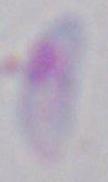

modality: micrograph
magnification: 1000x
identification: Toxoplasma gondii